Report the malaria status of this cell.
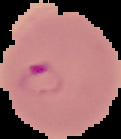

Parasitized.

Summary:
  - Image type: segmented cell region on a black background
  - Image size: 121×139 pixels
  - Preparation: thin blood film